Outline each blood parasite and name the species.
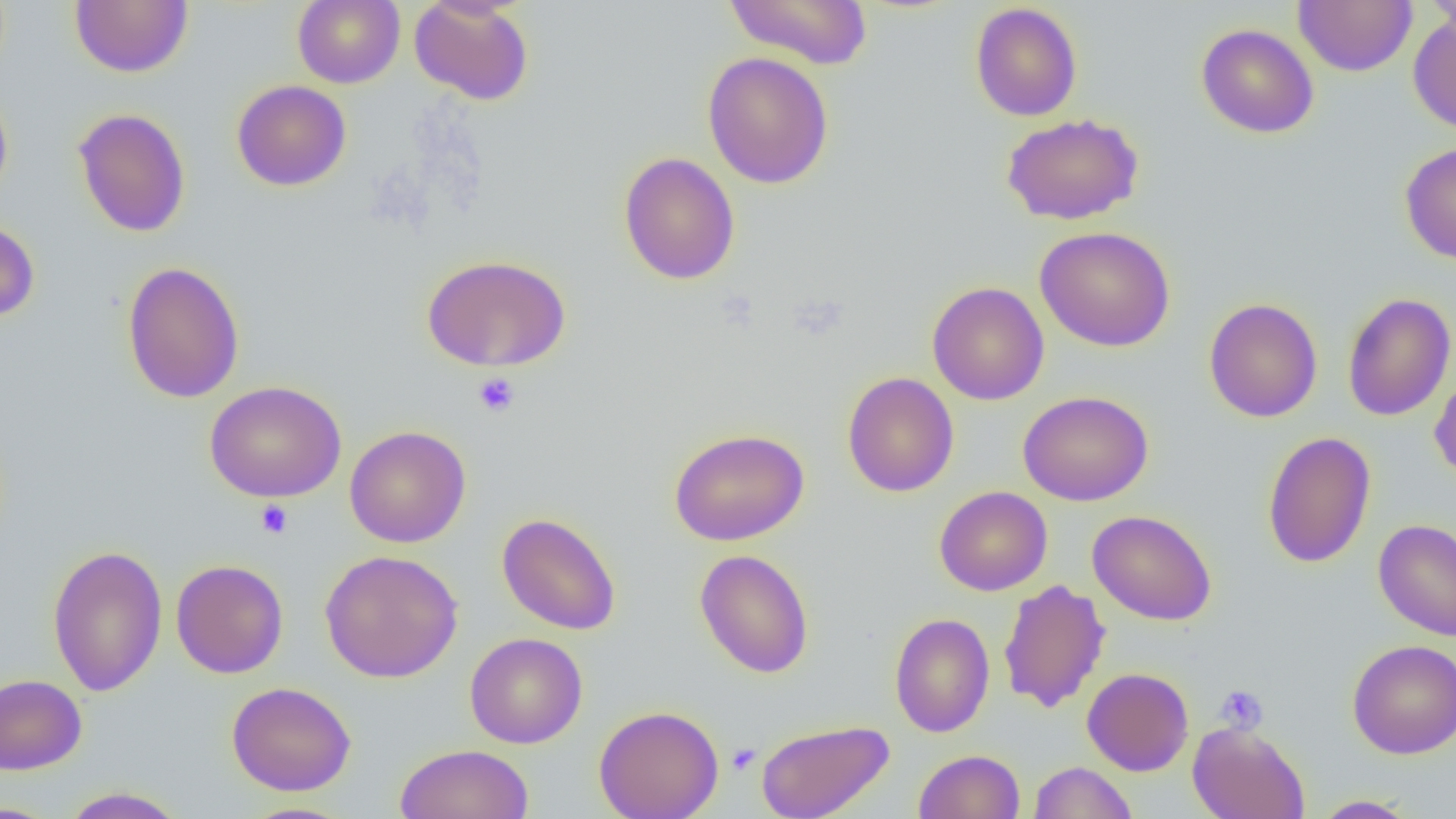
No blood parasites observed.

Approximate bounding boxes as (x1,y1)-(x2,y2) corner pairs in pixels. Platelet locations: (473,372)-(520,417), (256,500)-(293,538), (1215,684)-(1268,733), (726,743)-(760,775). Uninfected red blood cell locations: (69,0)-(193,78), (292,0)-(405,89), (409,0)-(534,105), (723,0)-(873,70), (1293,0)-(1417,76), (1423,0)-(1456,35), (970,3)-(1083,122), (1408,13)-(1456,135), (1196,23)-(1319,138), (702,51)-(834,189), (231,79)-(352,192), (0,86)-(13,206), (73,107)-(191,238), (1001,113)-(1144,225), (1399,141)-(1456,264), (618,152)-(741,285), (0,217)-(40,323), (1034,227)-(1175,352), (422,254)-(571,372), (121,261)-(245,403), (927,282)-(1050,405), (1342,292)-(1456,422), (1204,298)-(1323,423), (1429,369)-(1456,486), (842,372)-(959,497), (205,380)-(346,503), (1018,390)-(1154,506), (344,425)-(471,548), (669,428)-(809,546), (1262,431)-(1376,569), (934,486)-(1053,596), (1087,509)-(1217,626), (497,512)-(621,635), (1373,519)-(1456,641), (47,544)-(168,697), (695,548)-(814,678), (320,549)-(463,683), (171,559)-(289,678), (998,579)-(1110,714), (889,612)-(995,737), (465,631)-(588,749), (1347,639)-(1456,759), (1082,667)-(1194,776), (0,674)-(87,774), (226,681)-(356,796), (594,704)-(724,819), (756,719)-(895,819), (1187,720)-(1310,819), (395,743)-(533,819), (913,749)-(1025,819), (1028,760)-(1138,818), (58,786)-(189,818), (1310,794)-(1420,818), (0,801)-(62,818), (236,801)-(359,819). Slide-level diagnosis: no evidence of blood parasites. Captured at 1000x magnification. One field of a larger specimen. Thin blood film. Optical microscopy. Image is 1456×819 pixels.